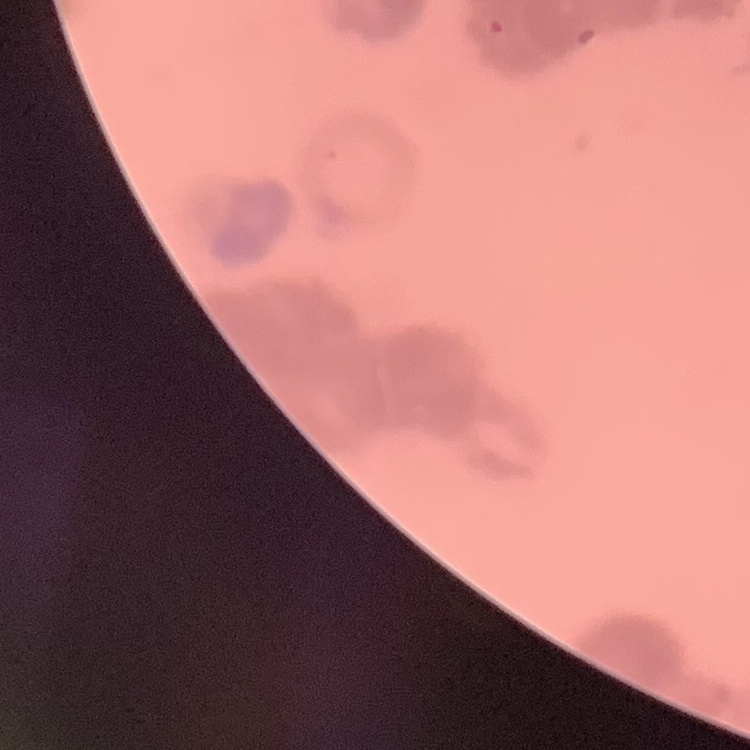
Summary:
  - Red blood cell morphology: rouleaux formation
  - Preparation: thin blood smear
  - Stain: Field's or Giemsa
  - Image type: one tile cut from a larger photomicrograph